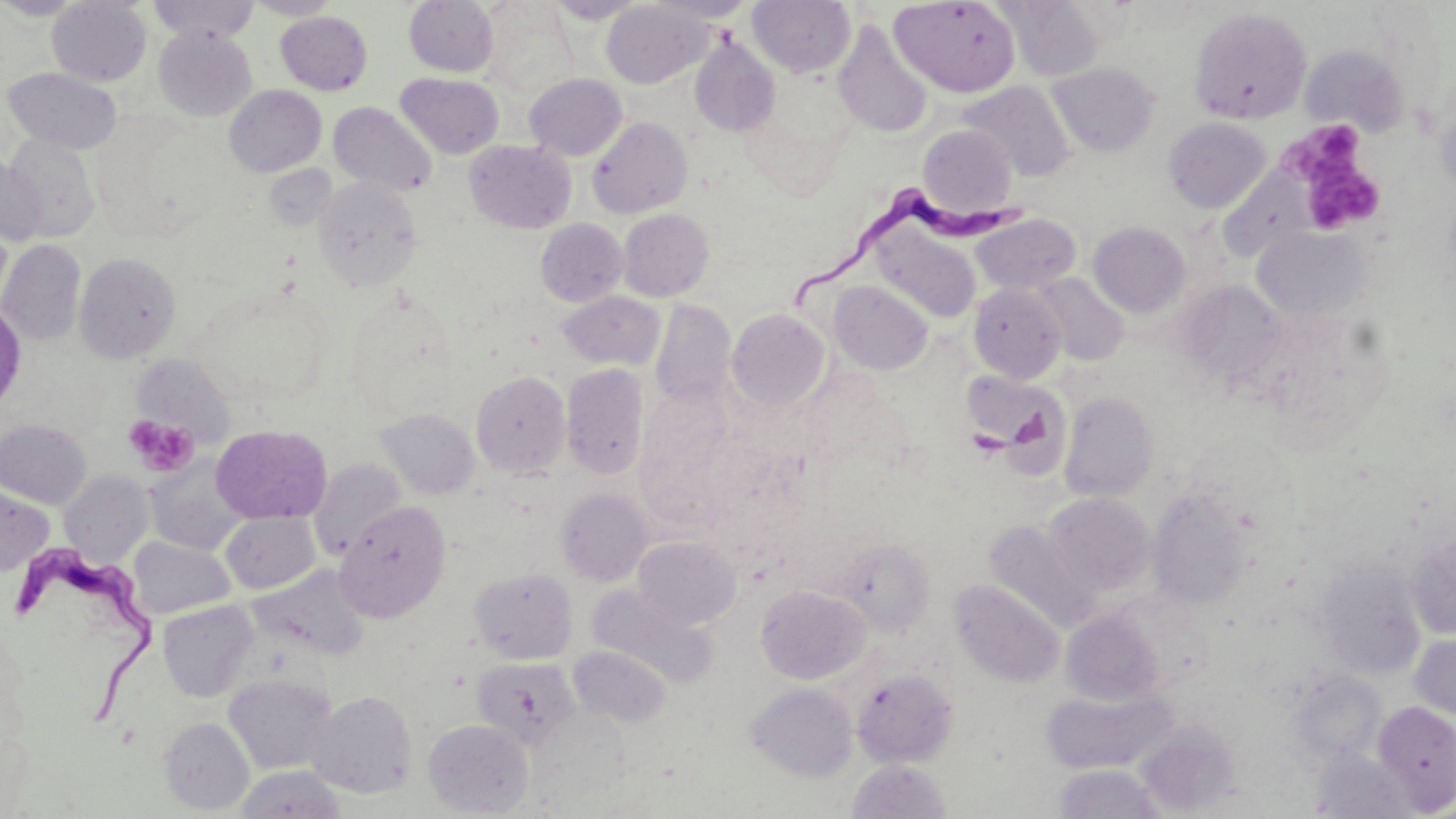
Summary:
  - Coordinate format: approximate bounding boxes as (x1,y1)-(x2,y2) corner pairs in pixels
  - Trypanosoma brucei locations: (790,184)-(1026,310), (12,540)-(157,731)
  - Platelet locations: (1284,118)-(1384,231), (124,415)-(198,477)
  - Uninfected red blood cell locations: (0,0)-(91,20), (147,0)-(260,43), (245,0)-(343,19), (404,0)-(499,77), (546,0)-(649,24), (647,0)-(757,22), (748,0)-(855,77), (890,0)-(1022,97), (1002,0)-(1105,81), (47,1)-(152,86), (601,2)-(713,88), (478,3)-(577,96), (1190,8)-(1312,124), (276,11)-(373,95), (833,22)-(933,138), (153,27)-(257,121), (689,35)-(780,137), (1299,43)-(1411,137), (1047,61)-(1160,156), (3,68)-(122,153), (395,72)-(504,159), (524,73)-(627,160), (960,81)-(1076,181), (224,85)-(326,177), (1435,91)-(1456,200), (329,102)-(437,197), (588,118)-(693,218), (1163,118)-(1271,213), (917,125)-(1018,215), (3,136)-(101,243), (465,140)-(576,234), (0,158)-(46,246), (1217,166)-(1316,260), (313,177)-(422,292), (618,208)-(714,301), (971,214)-(1081,294), (535,218)-(627,306), (1088,221)-(1191,318), (0,223)-(13,317), (1251,226)-(1372,322), (872,229)-(982,324), (0,240)-(86,346), (75,253)-(181,362), (1034,273)-(1129,366), (830,281)-(933,374), (1177,281)-(1291,389), (969,283)-(1067,384), (557,291)-(665,371), (650,299)-(736,408), (0,302)-(27,412), (726,309)-(831,413), (130,354)-(233,443), (561,364)-(649,480), (959,369)-(1066,455), (471,371)-(570,477), (1058,392)-(1159,502), (376,409)-(479,499), (0,419)-(91,509), (211,425)-(331,523), (146,458)-(250,555), (309,459)-(408,561), (60,470)-(153,565), (0,485)-(54,576), (556,488)-(652,587), (1148,490)-(1251,609), (1043,492)-(1155,596), (335,501)-(451,622), (221,511)-(320,594), (984,521)-(1100,630), (1407,532)-(1456,639), (633,536)-(742,629), (128,537)-(235,619), (836,538)-(935,635), (1316,559)-(1426,679), (249,566)-(369,658), (470,567)-(578,664), (951,580)-(1065,688), (756,585)-(869,685), (587,586)-(715,687), (158,601)-(257,701), (1060,608)-(1164,706), (1409,634)-(1456,722), (568,645)-(672,728), (472,656)-(579,750), (852,667)-(958,767), (1287,672)-(1386,764), (223,673)-(337,774), (746,682)-(857,781), (1040,685)-(1177,774), (307,690)-(417,798), (1372,700)-(1456,812), (159,717)-(254,814), (423,719)-(534,816), (1135,724)-(1240,815), (1310,749)-(1418,819), (848,760)-(952,818), (1052,764)-(1168,818), (236,766)-(345,819)
  - Slide-level diagnosis: Trypanosoma brucei
  - Image size: 1456×819 pixels
  - Modality: optical microscopy
  - Magnification: 1000x
  - Stain: May-Grünwald-Giemsa
  - Preparation: thin blood smear
  - Field of view: single